Classify this cell by malaria status.
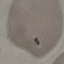

Uninfected.

stain = Giemsa
capture = smartphone camera at the microscope eyepiece
image type = cell patch, automatically extracted from a larger field of view and resized to 64 × 64 pixels
preparation = thin smear